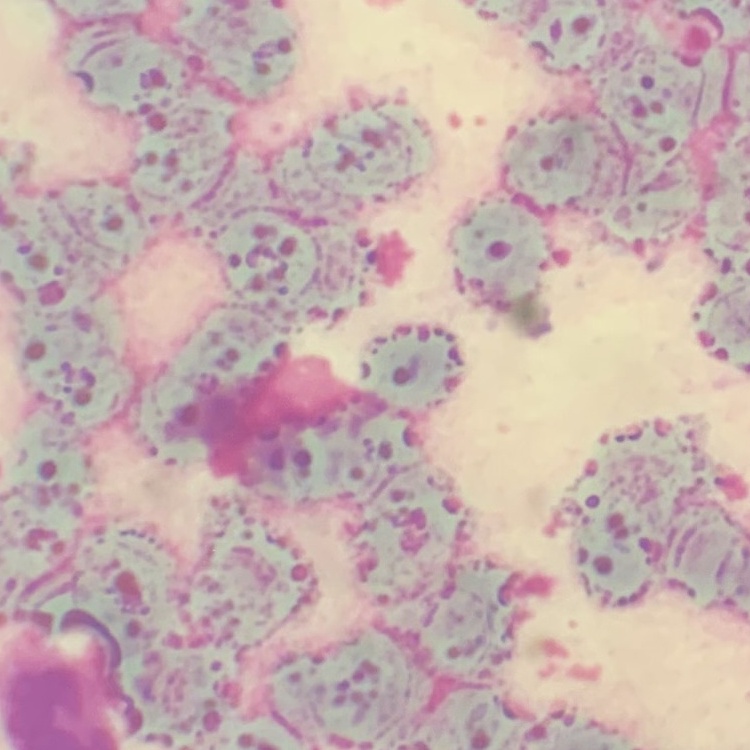

Summary:
  - Red blood cell morphology: rouleaux formation
  - Image type: square crop of a larger photomicrograph
  - Preparation: thin peripheral smear
  - Stain: Field's or Giemsa